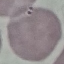 Result: negative for malaria parasites. Giemsa-stained preparation. Automatically extracted cell patch, resized to 64 × 64 pixels. Thin blood smear. Photographed with a smartphone camera at the microscope eyepiece.